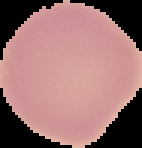
Summary:
  - Image size: 142×148 pixels
  - Result: no malaria parasites seen
  - Preparation: thin blood smear
  - Image type: cell region segmented out of the field of view; surrounding area masked to black